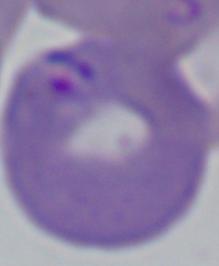
magnification = 1000x
modality = micrograph
identification = Babesia